Classify this cell by malaria status.
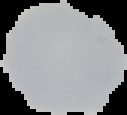
Uninfected.

From a thin blood film. The area outside the segmented cell region is set to black. Image is 127×115 pixels.